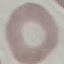

Summary:
  - Malaria status: uninfected
  - Image type: automatically extracted cell patch, resized to 64 × 64 pixels
  - Stain: Giemsa
  - Capture: smartphone camera at the microscope eyepiece
  - Preparation: thin blood smear